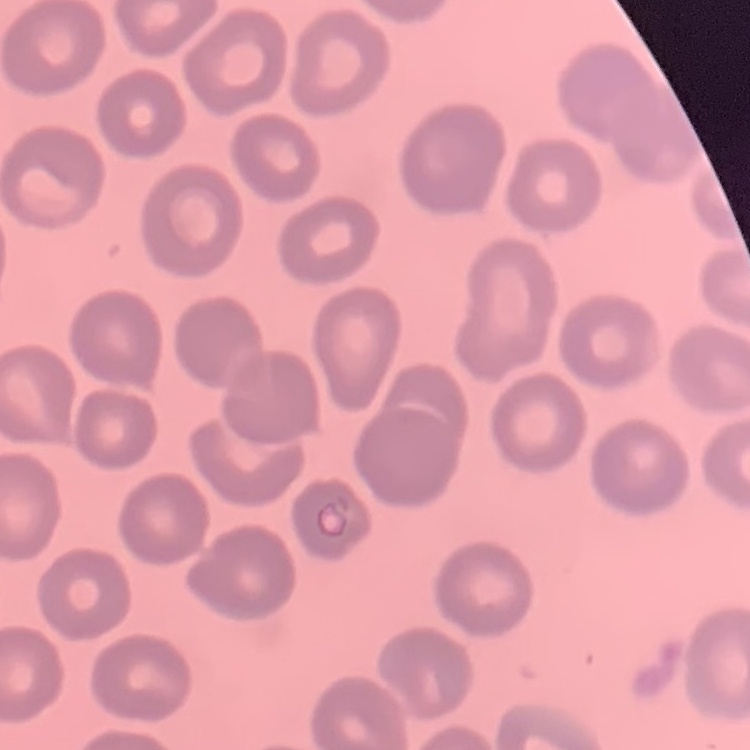
red_blood_cell_morphology: no rouleaux formation
preparation: thin peripheral smear
stain: Field's or Giemsa
image_type: one tile cut from a larger photomicrograph